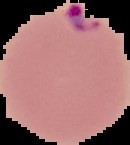
malaria_status: parasitized
preparation: thin blood smear
image_size: 130×145 pixels
image_type: segmented cell region with the area outside set to black